Report the malaria status of this cell.
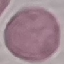
Uninfected.

capture: smartphone through the microscope eyepiece
image_type: automatically extracted cell patch, resized to 64 × 64 pixels
preparation: thin smear
stain: Giemsa